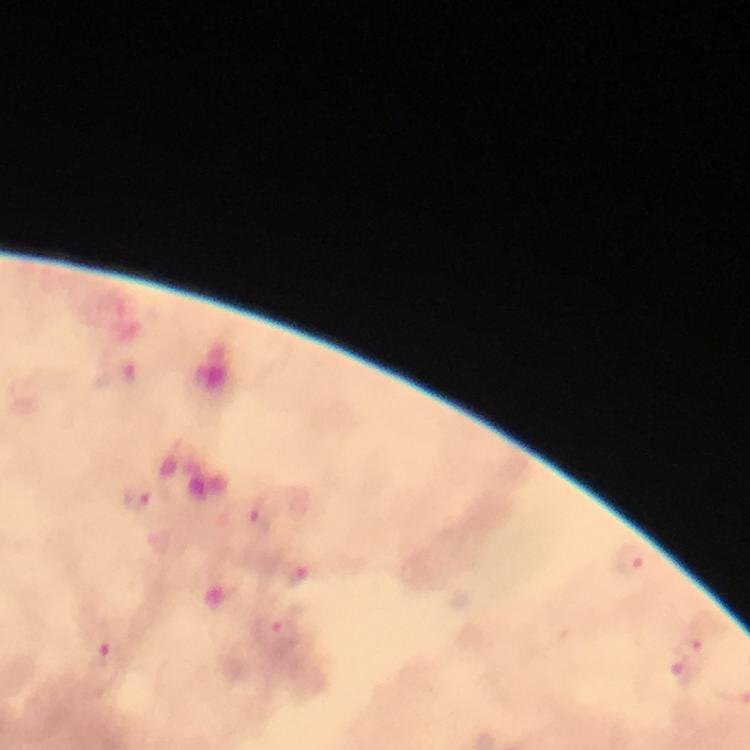

Approximate centers as {x, y} in pixels.
Summary:
  - Plasmodium parasite locations: {139, 498}, {260, 512}, {627, 560}, {296, 577}, {284, 631}, {689, 647}, {104, 657}, {686, 673}
  - Context: from a malaria diagnostic workup
  - Image size: 750×750 pixels
  - Preparation: thick blood film
  - Capture: smartphone camera through the microscope
  - Magnification: 100x
  - Stain: Giemsa
  - Cropped from: a single field of view
  - Immersion oil: used